Give the extent of all Plasmodium vivax-infected red blood cells.
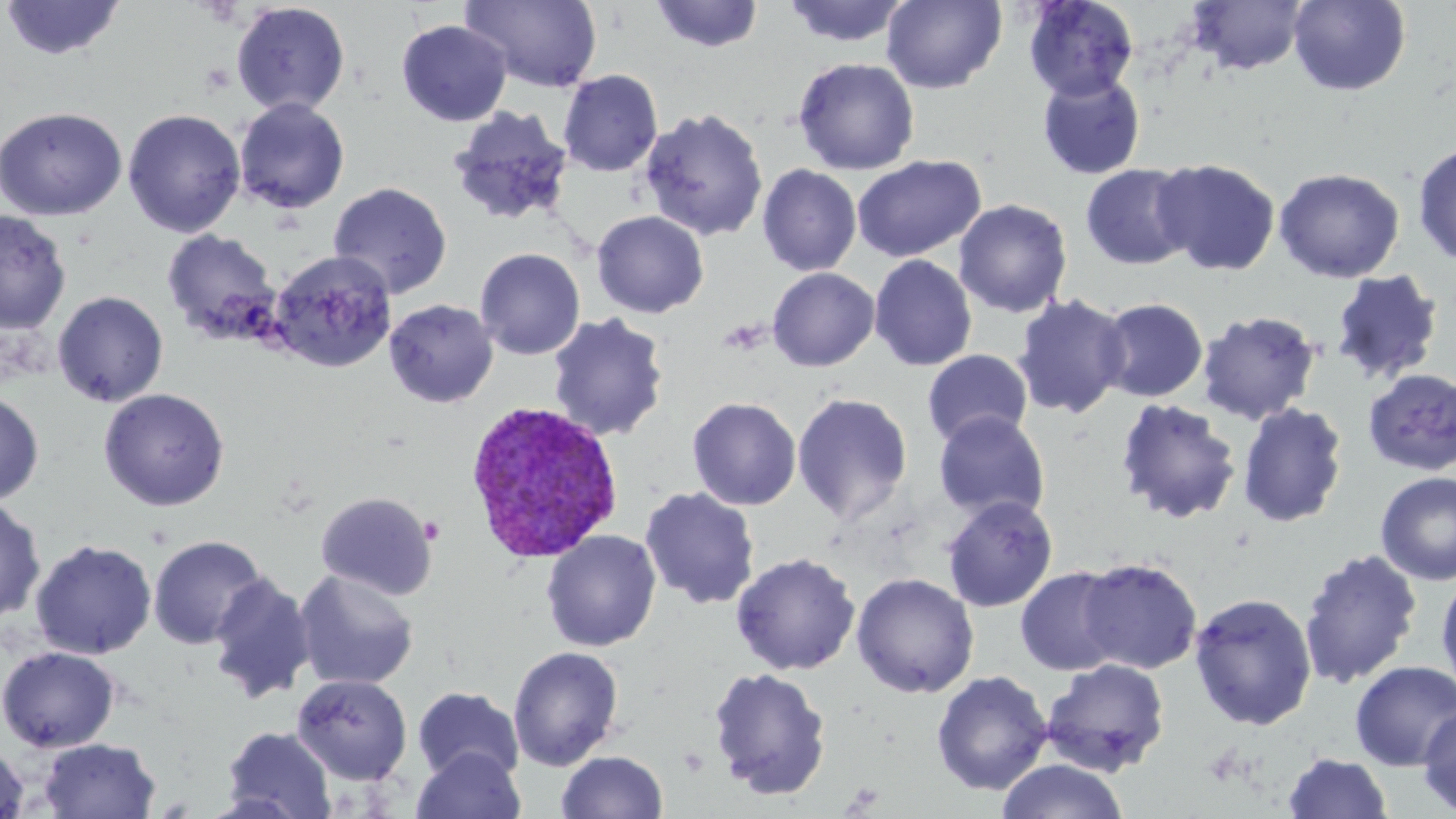

Approximate bounding boxes as (x1,y1)-(x2,y2) corner pairs in pixels.
Plasmodium vivax-infected red blood cells: (464,399)-(623,564).

Uninfected red blood cell locations: (461,0)-(603,93), (782,0)-(912,48), (882,0)-(1006,93), (1022,0)-(1140,102), (1186,0)-(1309,76), (1288,0)-(1411,96), (1,1)-(126,61), (650,1)-(763,53), (230,2)-(350,117), (396,19)-(511,126), (793,57)-(920,176), (558,69)-(663,177), (1036,72)-(1147,181), (233,98)-(350,213), (0,106)-(128,221), (447,107)-(574,227), (639,107)-(768,241), (123,108)-(246,237), (1412,142)-(1456,266), (852,154)-(985,262), (1153,157)-(1281,276), (1080,162)-(1198,270), (757,164)-(862,276), (1273,167)-(1405,283), (328,181)-(452,299), (953,198)-(1073,318), (0,210)-(71,333), (591,210)-(710,318), (162,228)-(282,344), (475,247)-(586,360), (268,251)-(397,372), (868,254)-(978,371), (767,267)-(879,370), (1329,269)-(1445,386), (52,290)-(169,407), (1012,293)-(1132,420), (1096,297)-(1208,402), (383,299)-(499,408), (1197,309)-(1322,426), (547,312)-(670,442), (922,349)-(1034,448), (1363,368)-(1456,476), (98,387)-(230,511), (0,390)-(44,507), (792,392)-(913,526), (687,396)-(802,510), (1114,397)-(1243,524), (1237,402)-(1348,527), (933,410)-(1051,522), (1375,471)-(1455,586), (639,487)-(761,610), (315,490)-(439,600), (942,495)-(1058,612), (0,497)-(45,626), (540,529)-(662,652), (148,534)-(268,650), (30,538)-(157,660), (1298,548)-(1422,688), (730,551)-(861,675), (1078,557)-(1203,674), (1015,566)-(1125,676), (294,569)-(419,691), (851,571)-(980,698), (1436,572)-(1456,697), (207,573)-(316,704), (1188,592)-(1318,730), (1,645)-(120,753), (507,645)-(625,771), (1041,658)-(1171,777), (1350,660)-(1456,770), (707,666)-(832,800), (931,670)-(1053,795), (291,673)-(413,785), (412,687)-(525,784), (1418,704)-(1456,816), (222,726)-(337,818), (37,738)-(161,818), (0,741)-(31,819), (412,746)-(526,819), (556,750)-(669,819), (1282,752)-(1393,818), (996,759)-(1129,819). Slide-level diagnosis: Plasmodium vivax. One field of a larger specimen. Optical microscopy. Image is 1456×819 pixels. 1000x magnification. Thin blood film. May-Grünwald-Giemsa-stained preparation.